Report the malaria status of this cell.
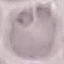
It is uninfected.

image_type: cell patch, automatically extracted from a larger field of view and resized to 64 × 64 pixels
capture: smartphone camera at the microscope eyepiece
preparation: thin blood smear
stain: Giemsa